Mark where platelets are.
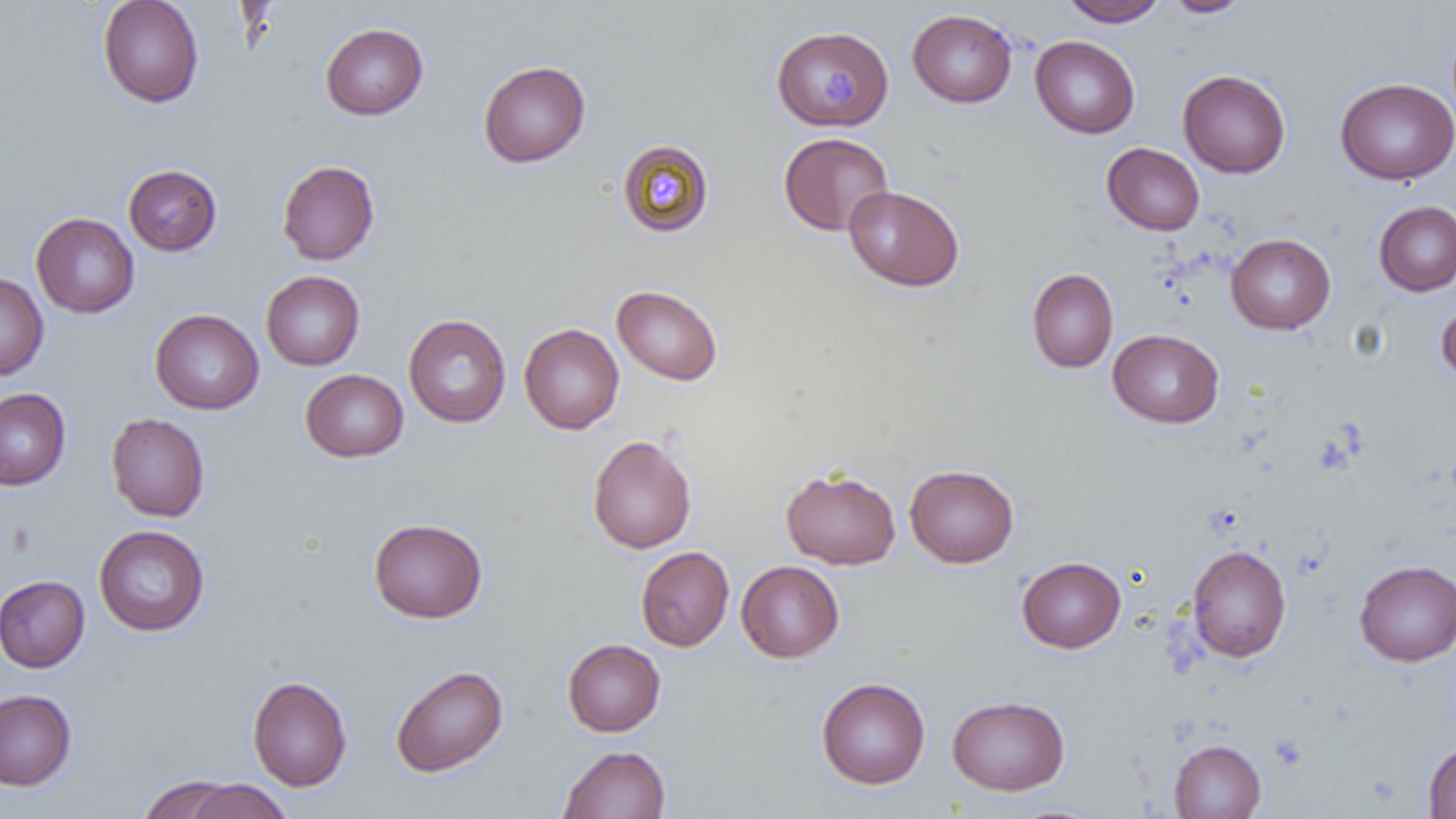
Approximate bounding boxes as [x1, y1, x2, y2] in pixels.
Platelets: [819, 71, 855, 110].

Summary:
  - Uninfected red blood cell locations: [97, 0, 204, 108], [1059, 0, 1168, 26], [1163, 0, 1252, 18], [907, 9, 1018, 108], [320, 22, 429, 120], [774, 25, 895, 131], [1030, 35, 1140, 138], [478, 60, 591, 168], [1178, 70, 1290, 178], [1335, 77, 1456, 185], [778, 132, 893, 236], [616, 138, 714, 237], [1101, 142, 1205, 235], [277, 160, 380, 265], [123, 164, 222, 256], [843, 185, 965, 292], [1373, 201, 1456, 296], [31, 212, 139, 318], [1225, 233, 1336, 334], [1026, 268, 1119, 373], [261, 271, 365, 371], [0, 272, 49, 380], [611, 285, 723, 386], [1436, 301, 1456, 387], [150, 309, 264, 414], [403, 314, 511, 428], [519, 323, 624, 434], [1108, 329, 1224, 428], [300, 369, 408, 462], [0, 388, 71, 490], [106, 413, 210, 522], [587, 434, 697, 553], [904, 464, 1019, 568], [780, 467, 901, 570], [368, 517, 488, 623], [94, 525, 210, 636], [1187, 544, 1291, 662], [635, 546, 734, 651], [1016, 556, 1126, 653], [736, 560, 844, 663], [1354, 560, 1456, 666], [0, 575, 90, 673], [562, 638, 665, 737], [390, 665, 508, 777], [247, 675, 352, 791], [816, 677, 930, 789], [0, 689, 77, 790], [947, 694, 1070, 795], [1169, 739, 1266, 818], [1423, 741, 1456, 818], [558, 745, 671, 818], [137, 774, 240, 818], [182, 779, 292, 819], [1001, 804, 1112, 819]
  - Slide-level diagnosis: no evidence of blood parasites
  - Preparation: thin blood film
  - Modality: light microscopy
  - Magnification: 1000x
  - Image size: 1456×819 pixels
  - Field of view: one of a larger specimen